Report the malaria status of this cell.
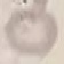

Uninfected.

Summary:
  - Preparation: thin blood film
  - Capture: smartphone through the microscope eyepiece
  - Stain: Giemsa
  - Image type: cell patch, automatically extracted from a larger field of view and resized to 64 × 64 pixels